Assess this cell for malaria.
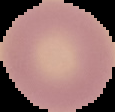
It is uninfected.

Image is 115×112 pixels. Segmented cell region on a black background. From a thin blood film.